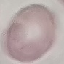 Malaria status: uninfected. Giemsa-stained preparation. Thin blood smear. Photographed with a smartphone camera at the microscope eyepiece. Automatically extracted cell patch, resized to 64 × 64 pixels.